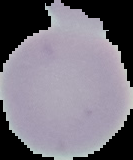
From a thin blood smear. Image is 133×160 pixels. Cell region segmented out of the field of view; the surrounding area is masked to black. Malaria status: uninfected.